Give the position of every malaria parasite.
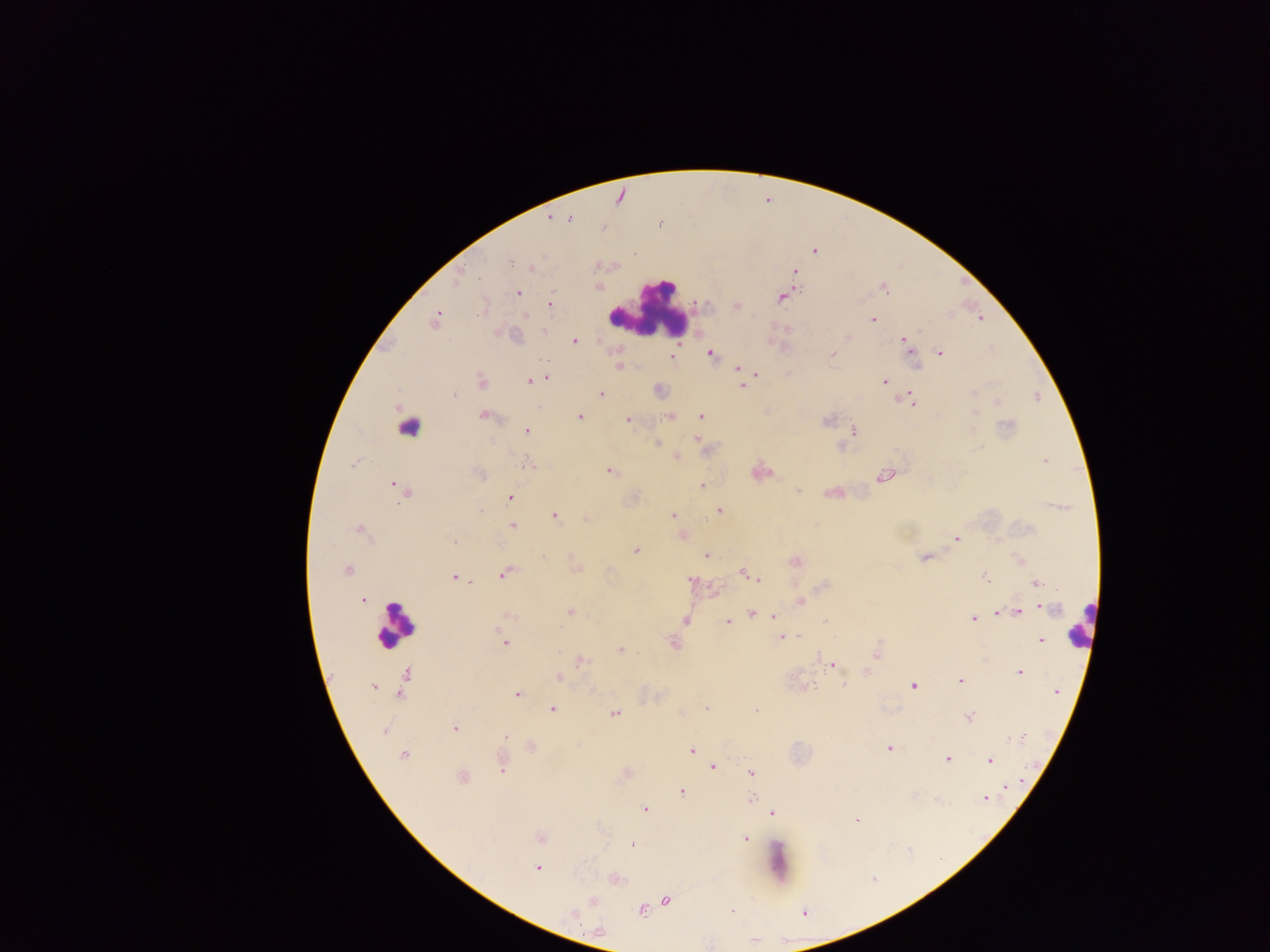
Approximate centers as x y in pixels.
Malaria parasites: 569 220; 510 262; 532 267; 795 271; 479 277; 599 286; 885 289; 517 293; 781 298; 551 302; 736 306; 484 308; 873 319; 980 319; 435 320; 544 332; 847 338; 905 340; 574 341; 940 352; 710 353; 833 354; 672 356; 619 366; 738 369; 756 375; 545 377; 481 381; 529 381; 884 381; 742 385; 973 392; 454 395; 601 395; 910 400; 997 402; 484 416; 701 416; 580 417; 670 417; 628 420; 827 420; 526 431; 854 431; 697 439; 657 443; 980 447; 678 458; 1045 461; 528 463; 353 465; 610 471; 480 474; 883 476; 396 486; 702 486; 404 490; 798 491; 514 492; 719 510; 480 511; 673 515; 555 516; 586 519; 513 526; 359 529; 956 538; 453 541; 636 551; 706 556; 543 557; 925 557; 796 562; 346 571; 743 572; 504 573; 749 575; 454 577; 985 577; 758 579; 691 580; 1036 583; 362 601; 800 601; 1051 608; 570 612; 1018 612; 752 613; 998 613; 509 616; 774 616; 972 619; 685 620; 728 621; 825 621; 799 636; 782 637; 1041 640; 505 643; 674 643; 619 650; 877 651; 580 660; 832 664; 1020 672; 558 678; 960 681; 844 685; 914 686; 373 687; 1057 691; 517 695; 707 708; 552 709; 756 711; 614 713; 969 716; 455 729; 384 730; 506 737; 1019 737; 890 748; 691 751; 403 755; 947 759; 990 761; 713 767; 501 770; 752 772; 462 777; 1008 786; 682 792; 751 798; 985 799; 645 809; 773 813; 856 820; 541 839; 745 839; 632 845; 537 868; 666 900; 593 901; 641 911; 732 911; 573 913.

Summary:
  - Leukocyte locations (subset; some below the resolvable size): 648 312; 414 425; 1080 623; 394 625; 781 862
  - Preparation: thick blood smear
  - Image size: 1270×952 pixels
  - Field of view: single
  - Capture: mobile-phone photograph through a microscope
  - Country: Ghana